Locate every P. falciparum parasite and identify its life-cycle stage.
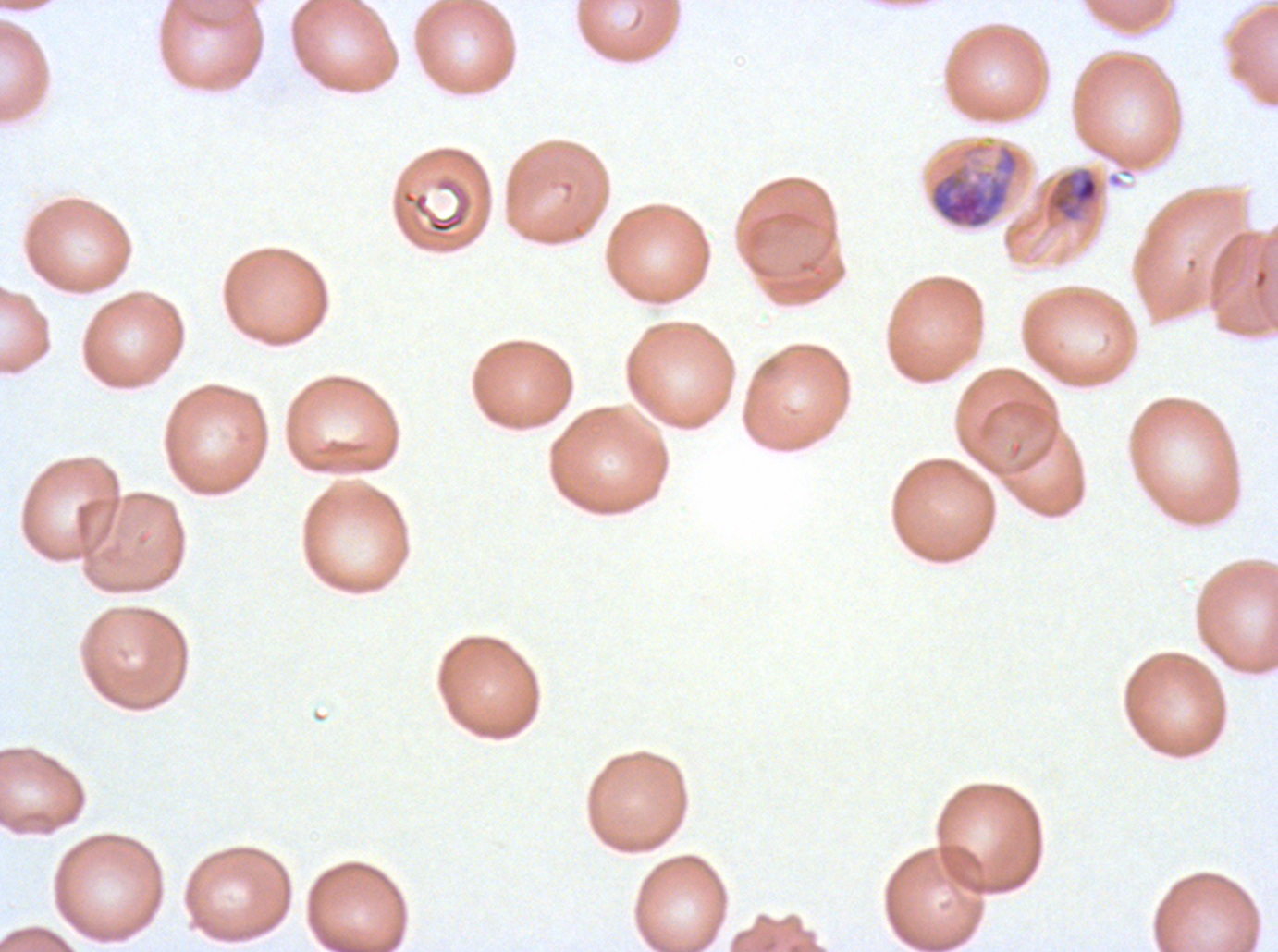

Approximate bounding boxes as {x1, y1, x2, y2} in pixels.
Late-ring/early-trophozoite forms: {1045, 166, 1100, 223}.
Early schizonts: {928, 139, 1027, 230}.
No rings, mid trophozoites, late trophozoites, late schizonts, segmenters, or gametocytes observed.

One sub-image of a larger composite. Giemsa stain. P. falciparum from a patient in The Gambia, cultured ex vivo for 24 to 48 hours. Thin blood film. Image is 1278×952 pixels. Life-cycle stages observed: late-ring/early-trophozoite, early schizont.